Classify this cell by malaria status.
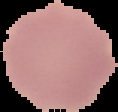
It is uninfected.

Summary:
  - Image size: 118×112 pixels
  - Preparation: thin blood smear
  - Image type: segmented cell region with the area outside set to black